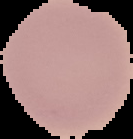
Summary:
  - Image type: segmented cell region on a black background
  - Result: no malaria parasites detected
  - Preparation: thin blood smear
  - Image size: 133×139 pixels